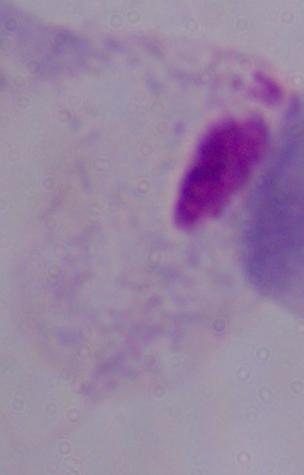
magnification = 1000x
modality = photomicrograph
identification = trichomonad